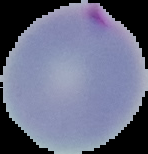
image type = cell region segmented out of the field of view; surrounding area masked to black
preparation = thin blood smear
malaria status = parasitized
image size = 148×154 pixels